Assess the morphology of the erythrocytes.
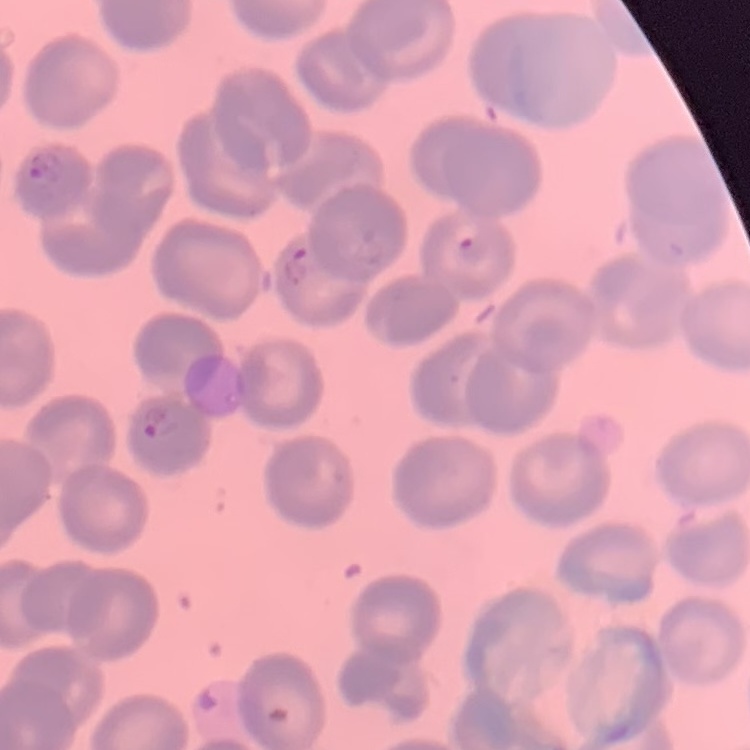
They show no rouleaux formation.

Summary:
  - Stain: Field's or Giemsa
  - Preparation: thin blood smear
  - Image type: one tile cut from a larger photomicrograph